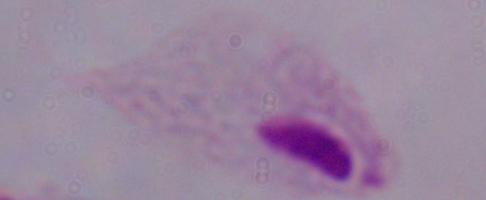

Summary:
  - Modality: micrograph
  - Identification: trichomonad
  - Magnification: 1000x